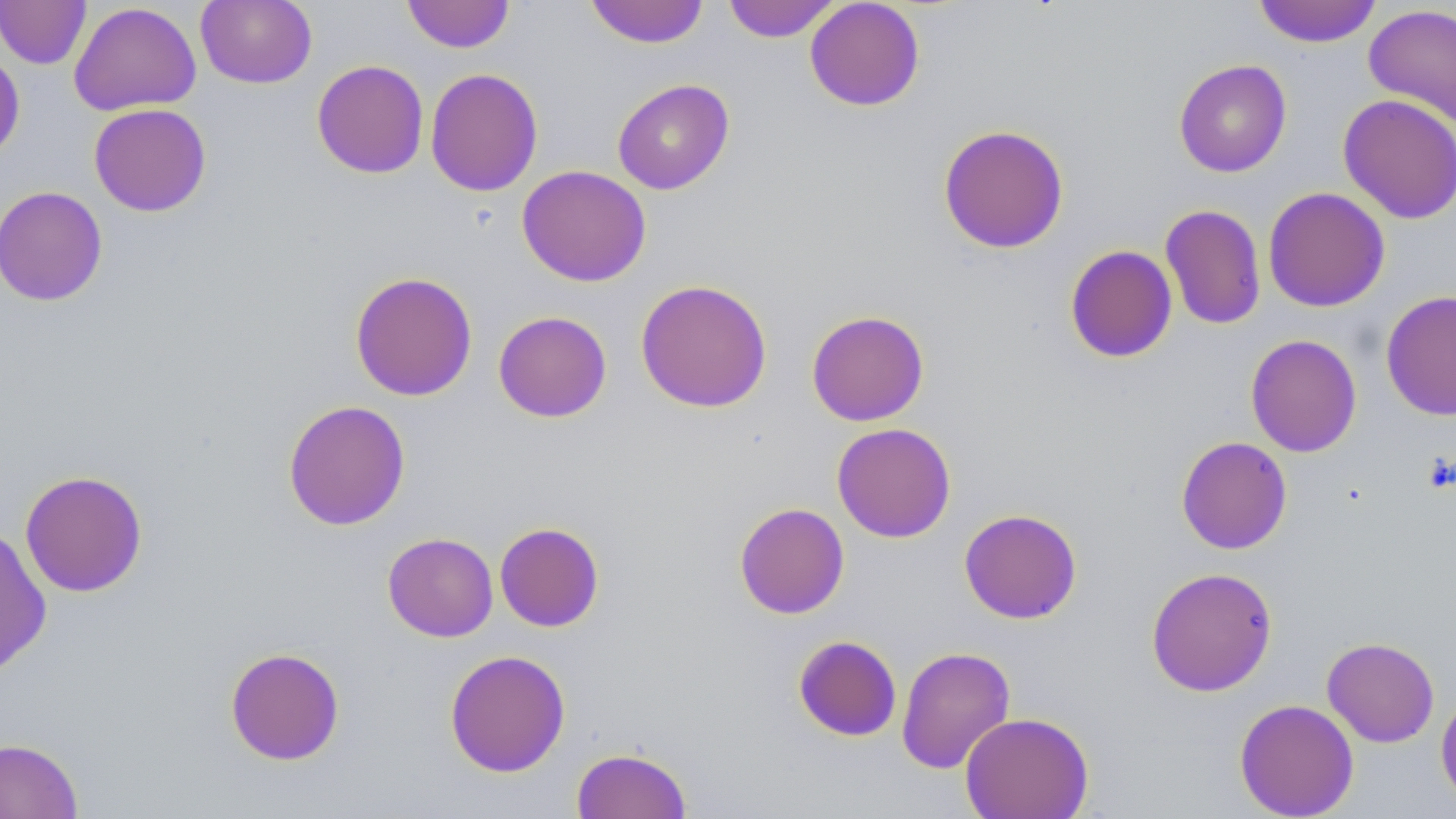
slide-level diagnosis = no evidence of blood parasites
stain = May-Grünwald-Giemsa
modality = optical microscopy
uninfected red blood cell locations = approximate bounding boxes as (x1, y1, x2, y2) in pixels: (196, 0, 317, 89), (402, 0, 516, 53), (585, 0, 710, 49), (723, 0, 841, 42), (805, 0, 925, 111), (0, 1, 91, 69), (1253, 1, 1383, 48), (68, 2, 201, 116), (1363, 4, 1456, 127), (0, 48, 25, 162), (311, 59, 429, 179), (1173, 59, 1292, 177), (425, 68, 543, 197), (612, 79, 735, 195), (1338, 94, 1456, 224), (88, 103, 212, 217), (937, 123, 1070, 254), (516, 165, 652, 287), (0, 186, 108, 306), (1262, 186, 1390, 312), (1159, 204, 1266, 330), (1064, 245, 1178, 363), (349, 271, 478, 401), (634, 279, 773, 413), (1381, 290, 1456, 421), (493, 310, 612, 423), (806, 310, 930, 426), (1245, 334, 1362, 457), (282, 399, 411, 531), (831, 422, 956, 543), (1176, 436, 1292, 554), (20, 470, 148, 597), (734, 502, 850, 619), (958, 508, 1083, 624), (494, 521, 604, 632), (0, 526, 52, 679), (382, 532, 498, 642), (1146, 566, 1278, 697), (793, 635, 902, 742), (1321, 637, 1440, 748), (896, 646, 1016, 774), (224, 647, 345, 765), (444, 649, 571, 777), (1435, 688, 1456, 807), (1234, 698, 1359, 818), (959, 712, 1094, 819), (0, 737, 83, 819), (571, 746, 692, 819)
field of view = one of a larger specimen
magnification = 1000x
preparation = thin blood film
image size = 1456×819 pixels